Assess the morphology of the erythrocytes.
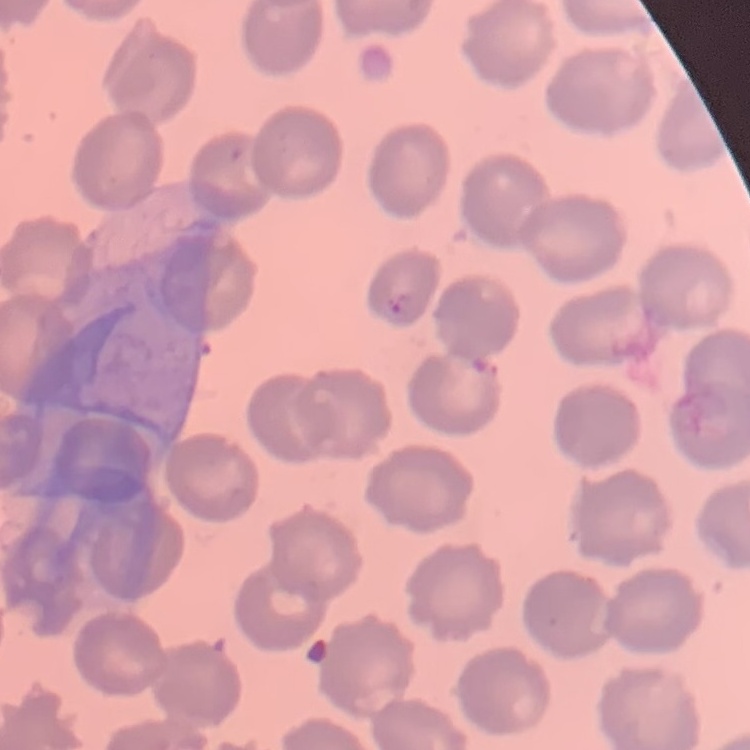

They show no rouleaux formation.

stain = Field's or Giemsa
image type = square crop of a larger photomicrograph
preparation = thin blood film